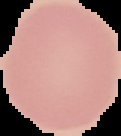 Segmented cell region on a black background. Image is 121×136 pixels. From a thin blood smear. Result: negative for Plasmodium parasites.